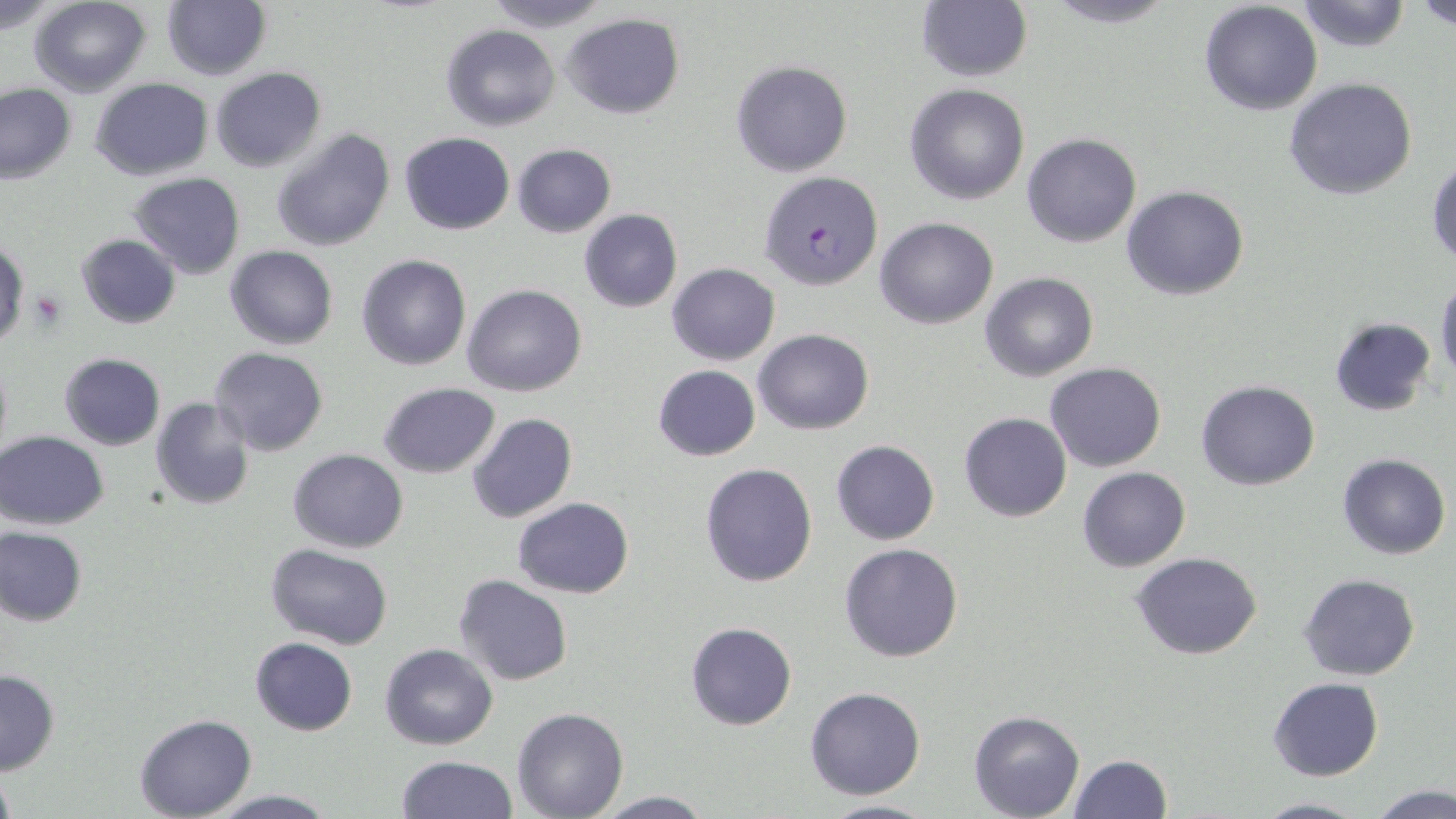
Approximate bounding boxes as (x1,y1)-(x2,y2) corner pairs in pixels. Uninfected red blood cell locations: (29,0)-(149,96), (481,0)-(615,32), (917,0)-(1032,83), (1040,0)-(1179,28), (1295,0)-(1413,54), (1415,0)-(1456,31), (1,1)-(66,34), (161,1)-(270,81), (1198,2)-(1323,116), (562,14)-(685,119), (441,23)-(560,131), (731,60)-(853,178), (211,66)-(326,172), (90,77)-(213,181), (1283,77)-(1417,202), (904,82)-(1032,205), (0,84)-(75,184), (271,127)-(397,252), (398,133)-(516,235), (1022,133)-(1141,247), (511,143)-(617,237), (1428,159)-(1456,267), (129,173)-(246,279), (1121,184)-(1249,300), (578,210)-(683,312), (875,217)-(998,329), (76,233)-(181,329), (0,234)-(29,350), (225,245)-(337,349), (356,254)-(471,371), (667,263)-(780,365), (980,272)-(1099,383), (1435,276)-(1456,388), (462,283)-(587,397), (1329,317)-(1436,417), (753,327)-(874,434), (210,347)-(327,456), (0,351)-(12,463), (59,353)-(165,450), (1046,361)-(1166,472), (653,364)-(760,461), (1196,380)-(1321,491), (379,381)-(500,478), (151,397)-(256,510), (959,412)-(1072,522), (465,413)-(578,525), (0,431)-(108,530), (830,439)-(940,545), (288,448)-(407,554), (1338,454)-(1450,559), (700,462)-(819,587), (1077,467)-(1190,571), (513,496)-(634,598), (486,505)-(615,649), (0,527)-(87,627), (265,543)-(395,648), (840,543)-(965,663), (1131,553)-(1263,659), (1299,572)-(1420,680), (453,573)-(573,686), (686,622)-(797,730), (250,637)-(358,735), (379,643)-(499,750), (1,669)-(60,775), (1268,678)-(1382,782), (805,686)-(927,800), (511,708)-(629,819), (968,708)-(1085,818), (134,714)-(256,818), (1068,753)-(1173,818), (395,754)-(518,819), (0,768)-(17,819), (1368,784)-(1455,819), (205,790)-(340,818), (589,791)-(717,818), (1252,794)-(1365,818), (818,797)-(938,818). Plasmodium falciparum-infected red blood cell locations: (760,171)-(880,291). Platelet locations: (32,289)-(67,333). Slide-level diagnosis: Plasmodium falciparum. Light microscopy. Image is 1456×819 pixels. One field of a larger specimen. Captured at 1000x magnification. May-Grünwald-Giemsa-stained preparation. Thin blood film.